Assess this cell for malaria.
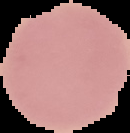

Uninfected.

Cell region segmented out of the field of view; the surrounding area is masked to black. Image is 130×133 pixels. From a thin blood film.